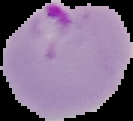
Cell region segmented out of the field of view; the surrounding area is masked to black. From a thin blood smear. Malaria status: parasitized. Image is 133×121 pixels.